Classify this cell by malaria status.
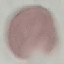

Uninfected.

Summary:
  - Preparation: thin blood film
  - Image type: automatically extracted cell patch, resized to 64 × 64 pixels
  - Stain: Giemsa
  - Capture: smartphone camera at the microscope eyepiece